Classify this cell by malaria status.
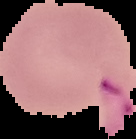

It is uninfected.

Segmented cell region on a black background. Image is 136×139 pixels. From a thin blood smear.